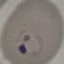

result = malaria parasites detected
preparation = thin smear
capture = smartphone camera at the microscope eyepiece
image type = cell patch, automatically extracted from a larger field of view and resized to 64 × 64 pixels
stain = Giemsa